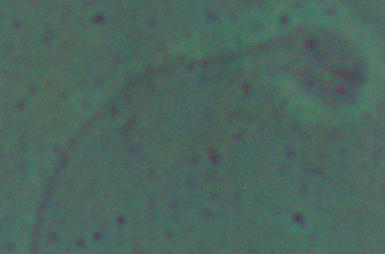
Summary:
  - Magnification: 1000x
  - Identification: Leishmania
  - Modality: photomicrograph